Classify this cell by malaria status.
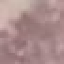

Uninfected.

stain = Giemsa
capture = smartphone camera at the microscope eyepiece
preparation = thin smear
image type = cell patch, automatically extracted from a larger field of view and resized to 64 × 64 pixels